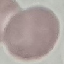
Summary:
  - Malaria status: uninfected
  - Preparation: thin blood smear
  - Stain: Giemsa
  - Image type: cell patch, automatically extracted from a larger field of view and resized to 64 × 64 pixels
  - Capture: smartphone through the microscope eyepiece